Give the position of every leukocyte visible.
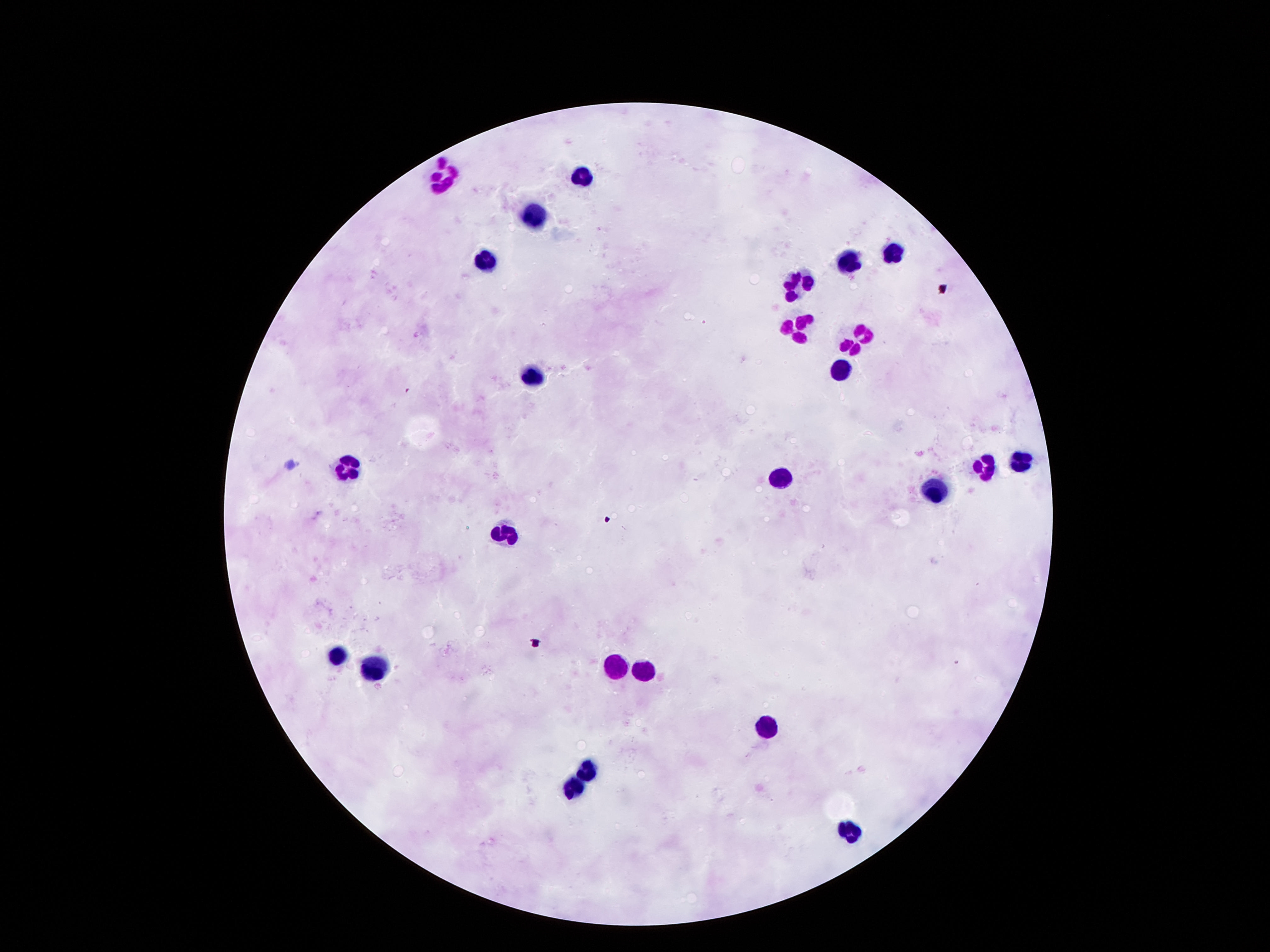

Approximate centers as {x, y} in pixels.
Leukocytes: {448, 173}, {575, 177}, {530, 214}, {894, 247}, {485, 258}, {849, 260}, {800, 280}, {794, 333}, {853, 337}, {840, 363}, {532, 375}, {350, 460}, {1021, 461}, {984, 465}, {782, 478}, {934, 490}, {509, 536}, {336, 648}, {374, 660}, {614, 664}, {645, 665}, {768, 726}, {588, 762}, {573, 785}, {847, 833}.

Image is 1270×952 pixels. Thick blood smear. Giemsa stain. Single field of view. 100x magnification. Smartphone photograph taken through the microscope eyepiece. Patient malaria status: negative.